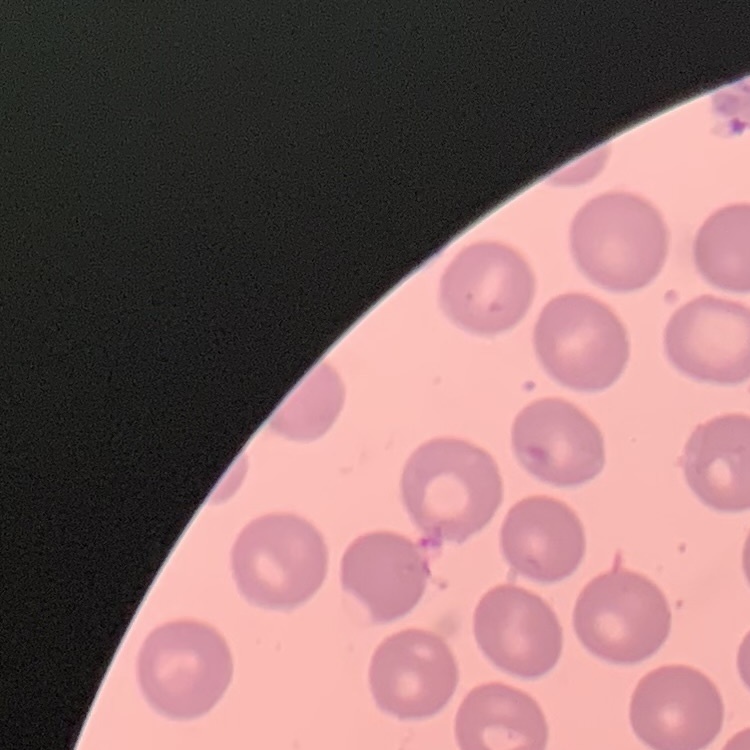

The red blood cells show no rouleaux formation. Field's or Giemsa stain. One tile cut from a larger photomicrograph. Thin blood film.